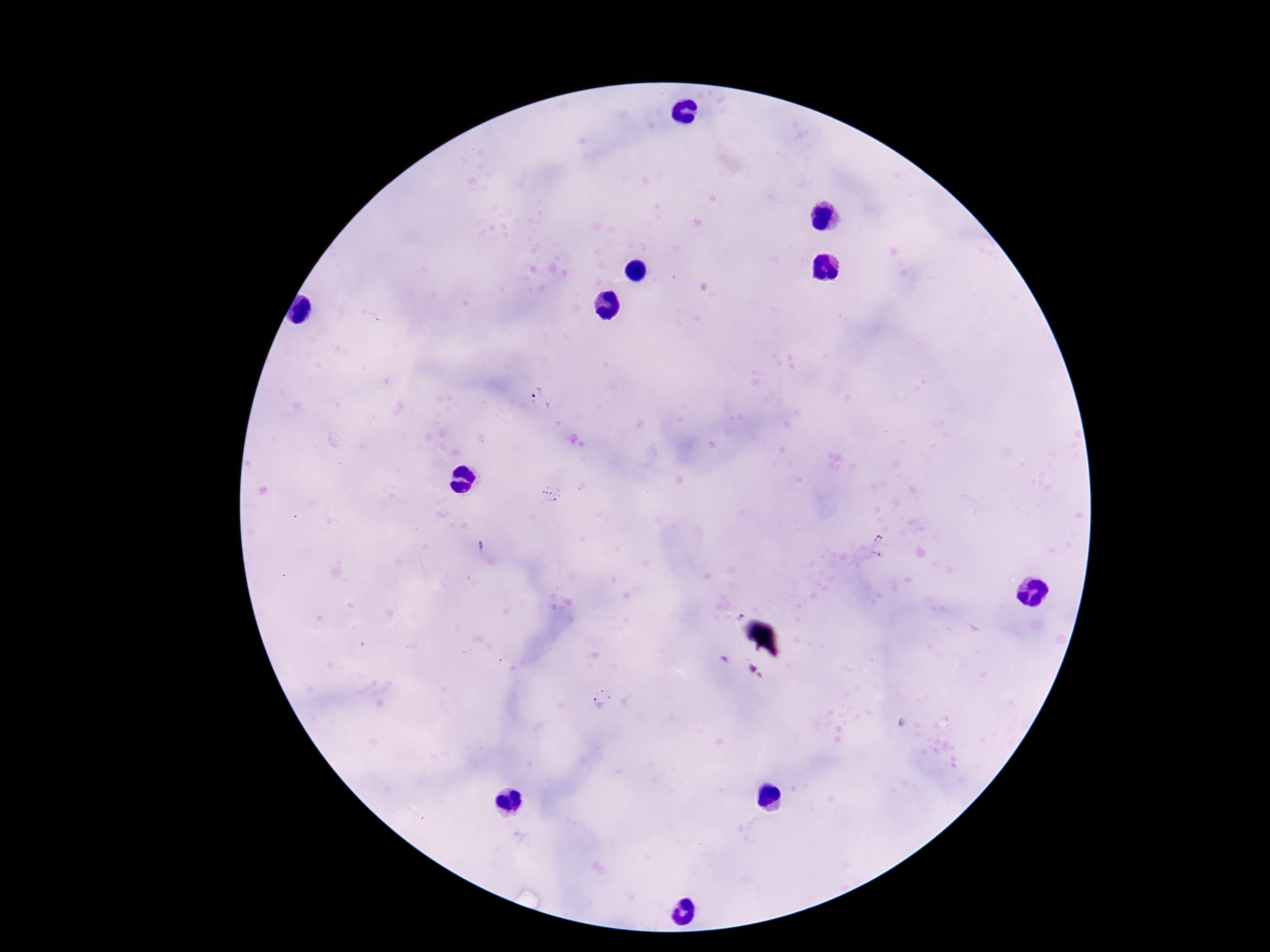

Approximate centers as {x, y} in pixels.
Summary:
  - Plasmodium parasite locations: {541, 400}, {551, 495}, {481, 545}, {736, 617}, {601, 696}
  - Magnification: 100x
  - Field of view: one from this slide
  - Capture: smartphone camera through the microscope eyepiece
  - Patient malaria status: positive
  - Image size: 1270×952 pixels
  - Stain: Giemsa
  - Preparation: thick blood film